State which parasite is depicted.
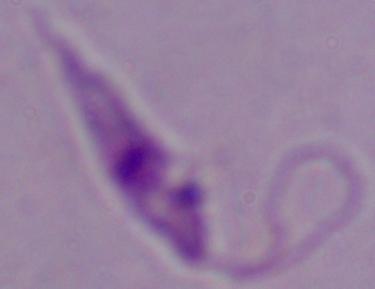

Leishmania.

{
  "modality": "photomicrograph",
  "magnification": "1000x"
}